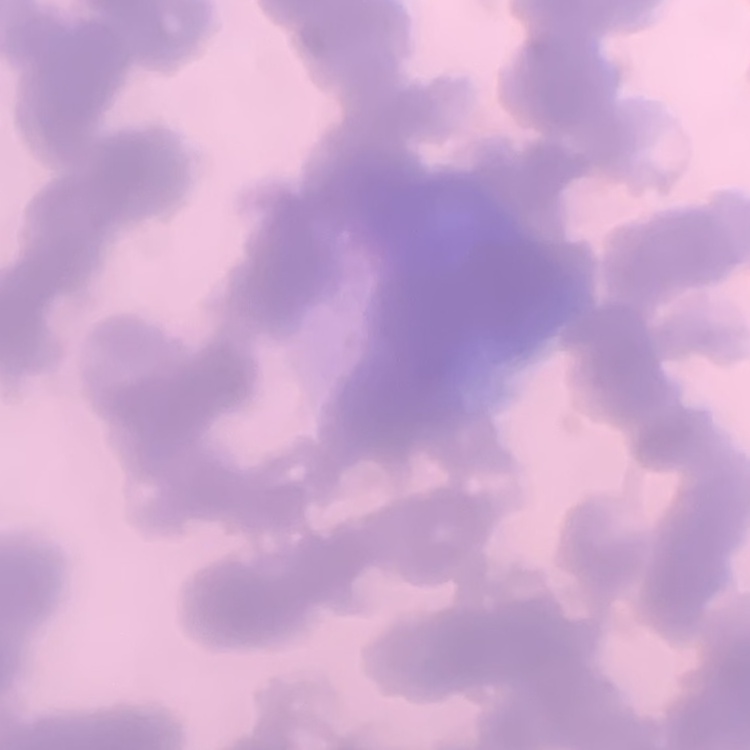
Summary:
  - Erythrocyte morphology: rouleaux formation
  - Preparation: thin blood film
  - Image type: one tile cut from a larger photomicrograph
  - Stain: Field's or Giemsa